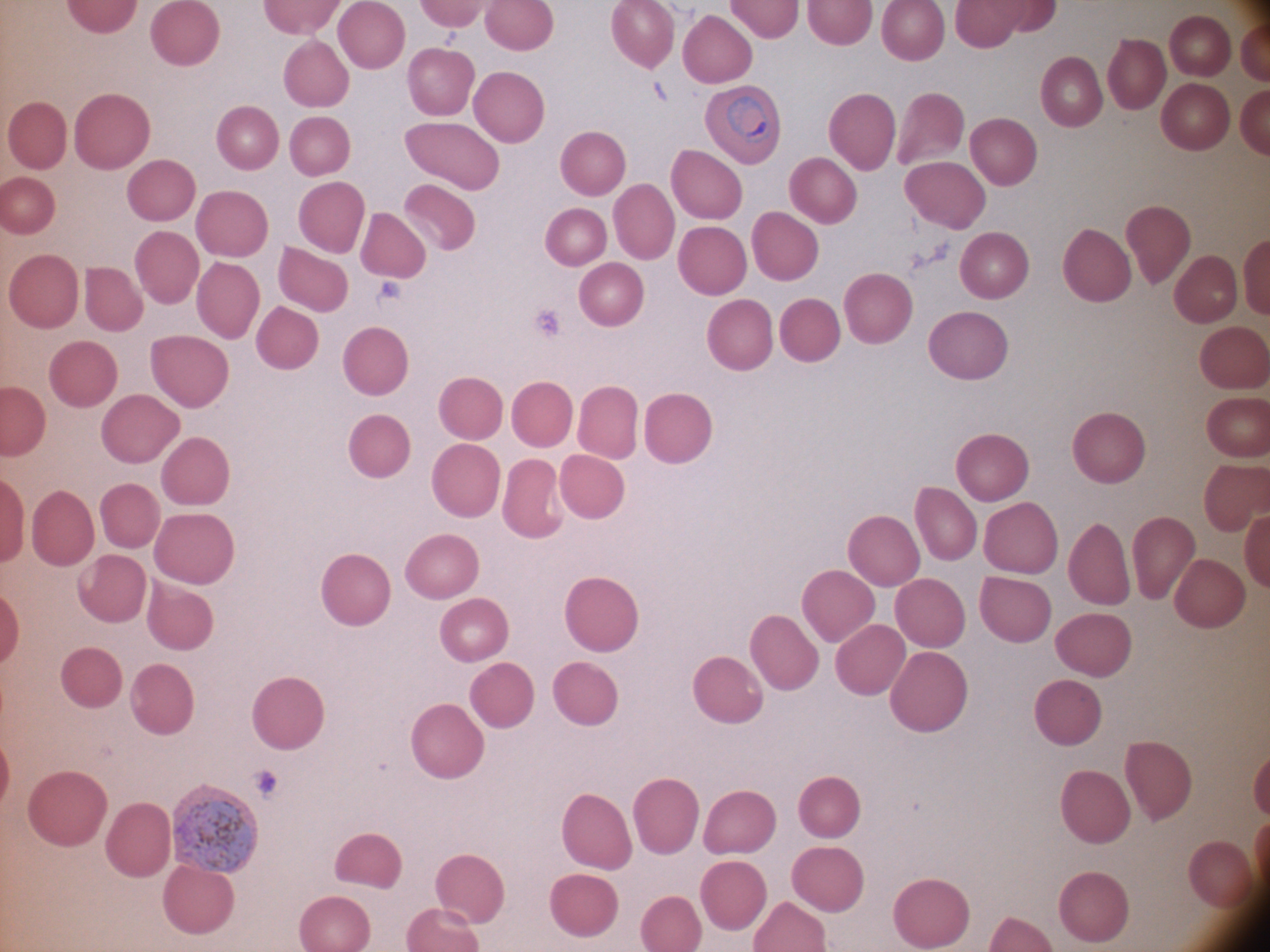

Approximate bounding boxes as [x1, y1, x2, y2] in pixels, from the source annotation, which is not necessarily exhaustive. Malaria parasite locations: [725, 95, 772, 146], [173, 799, 255, 875]. Life-cycle stages among the annotated parasites: ring form, trophozoite. Giemsa-stained preparation. Acquired with a Leica DM2000 optical microscope and its built-in camera. Captured at 100x magnification. Species: Plasmodium ovale. Image is 1270×952 pixels. Thin blood smear. Single field of view.